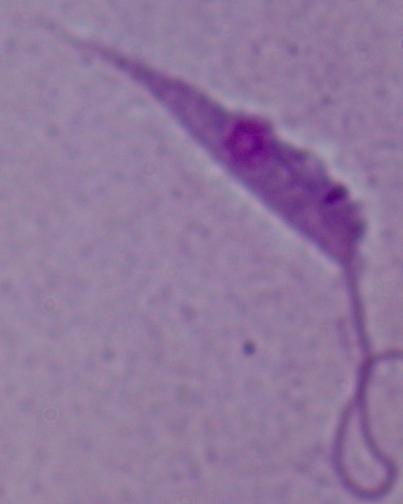
{
  "modality": "photomicrograph",
  "magnification": "1000x",
  "identification": "Leishmania"
}